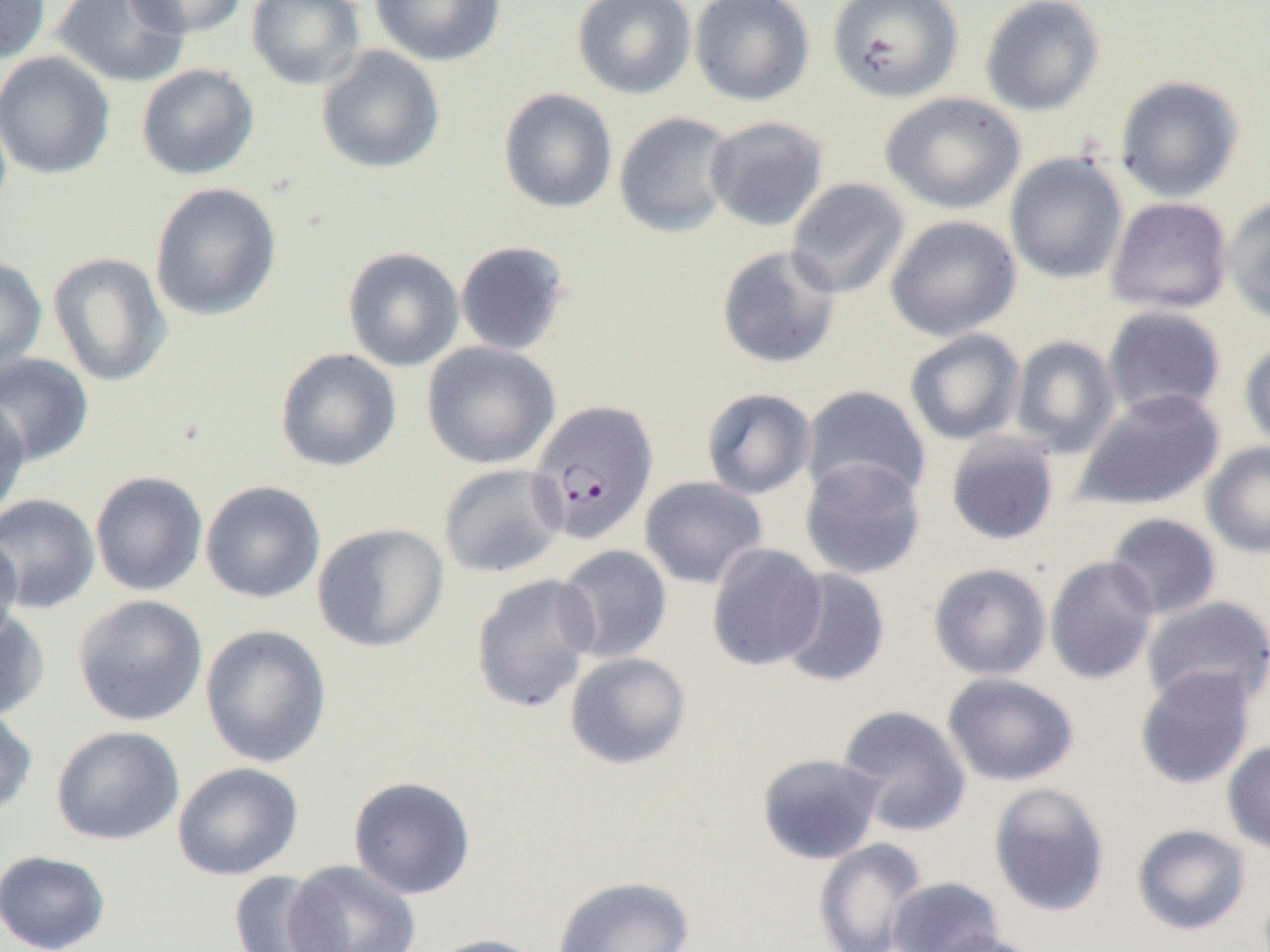

{
  "slide_level_diagnosis": "Plasmodium falciparum",
  "modality": "optical microscopy",
  "magnification": "1000x",
  "preparation": "thin blood smear",
  "uninfected_red_blood_cell_locations": "approximate bounding boxes as named x1/y1/x2/y2 corners in pixels: (x1=0, y1=0, x2=50, y2=63), (x1=52, y1=0, x2=190, y2=88), (x1=124, y1=0, x2=250, y2=38), (x1=246, y1=0, x2=365, y2=90), (x1=369, y1=0, x2=506, y2=66), (x1=572, y1=0, x2=696, y2=99), (x1=689, y1=0, x2=815, y2=106), (x1=827, y1=0, x2=962, y2=104), (x1=980, y1=0, x2=1104, y2=116), (x1=315, y1=45, x2=445, y2=174), (x1=0, y1=51, x2=115, y2=179), (x1=136, y1=63, x2=258, y2=179), (x1=1115, y1=76, x2=1244, y2=202), (x1=498, y1=88, x2=618, y2=214), (x1=880, y1=91, x2=1025, y2=214), (x1=614, y1=111, x2=736, y2=238), (x1=705, y1=115, x2=829, y2=231), (x1=1004, y1=153, x2=1128, y2=284), (x1=785, y1=177, x2=910, y2=299), (x1=150, y1=182, x2=282, y2=321), (x1=1223, y1=195, x2=1270, y2=323), (x1=1105, y1=197, x2=1233, y2=314), (x1=885, y1=214, x2=1021, y2=341), (x1=455, y1=240, x2=572, y2=356), (x1=716, y1=245, x2=842, y2=369), (x1=342, y1=246, x2=464, y2=372), (x1=47, y1=251, x2=173, y2=387), (x1=0, y1=254, x2=47, y2=376), (x1=1102, y1=305, x2=1227, y2=420), (x1=904, y1=328, x2=1026, y2=446), (x1=1010, y1=335, x2=1122, y2=458), (x1=1240, y1=339, x2=1270, y2=454), (x1=422, y1=342, x2=560, y2=469), (x1=274, y1=348, x2=401, y2=472), (x1=0, y1=353, x2=94, y2=466), (x1=801, y1=385, x2=932, y2=503), (x1=701, y1=387, x2=817, y2=499), (x1=1073, y1=388, x2=1225, y2=510), (x1=0, y1=394, x2=30, y2=522), (x1=944, y1=432, x2=1060, y2=546), (x1=1202, y1=441, x2=1270, y2=559), (x1=799, y1=457, x2=927, y2=580), (x1=438, y1=463, x2=567, y2=578), (x1=89, y1=471, x2=208, y2=597), (x1=639, y1=476, x2=768, y2=589), (x1=200, y1=480, x2=326, y2=603), (x1=0, y1=493, x2=100, y2=614), (x1=1105, y1=513, x2=1222, y2=620), (x1=312, y1=522, x2=449, y2=653), (x1=0, y1=533, x2=23, y2=647), (x1=706, y1=543, x2=827, y2=671), (x1=555, y1=544, x2=672, y2=663), (x1=1044, y1=555, x2=1160, y2=684), (x1=928, y1=562, x2=1051, y2=681), (x1=777, y1=568, x2=891, y2=687), (x1=470, y1=573, x2=599, y2=714), (x1=73, y1=594, x2=208, y2=726), (x1=1142, y1=595, x2=1270, y2=711), (x1=0, y1=609, x2=49, y2=722), (x1=199, y1=623, x2=332, y2=768), (x1=564, y1=652, x2=691, y2=769), (x1=1134, y1=667, x2=1256, y2=790), (x1=942, y1=672, x2=1080, y2=786), (x1=836, y1=704, x2=972, y2=837), (x1=0, y1=708, x2=37, y2=819), (x1=50, y1=725, x2=185, y2=845), (x1=1222, y1=739, x2=1270, y2=855), (x1=756, y1=753, x2=885, y2=865), (x1=171, y1=762, x2=304, y2=880), (x1=348, y1=776, x2=476, y2=900), (x1=988, y1=781, x2=1111, y2=917), (x1=1132, y1=823, x2=1252, y2=935), (x1=813, y1=838, x2=929, y2=952), (x1=0, y1=849, x2=110, y2=952), (x1=285, y1=860, x2=421, y2=952), (x1=229, y1=870, x2=341, y2=952), (x1=551, y1=876, x2=695, y2=952), (x1=886, y1=876, x2=1005, y2=952), (x1=424, y1=934, x2=553, y2=952), (x1=925, y1=934, x2=1047, y2=952)",
  "image_size": "1270×952 pixels",
  "plasmodium_falciparum_infected_red_blood_cell_locations": "approximate bounding boxes as named x1/y1/x2/y2 corners in pixels: (x1=526, y1=399, x2=659, y2=544)",
  "field_of_view": "one of a larger specimen"
}